Identify the cell.
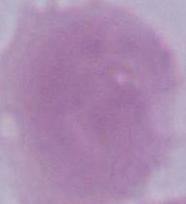

An erythrocyte.

1000x magnification. Photomicrograph.